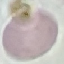
result = no malaria parasites seen
stain = Giemsa
capture = smartphone through the microscope eyepiece
preparation = thin blood smear
image type = cell patch, automatically extracted from a larger field of view and resized to 64 × 64 pixels